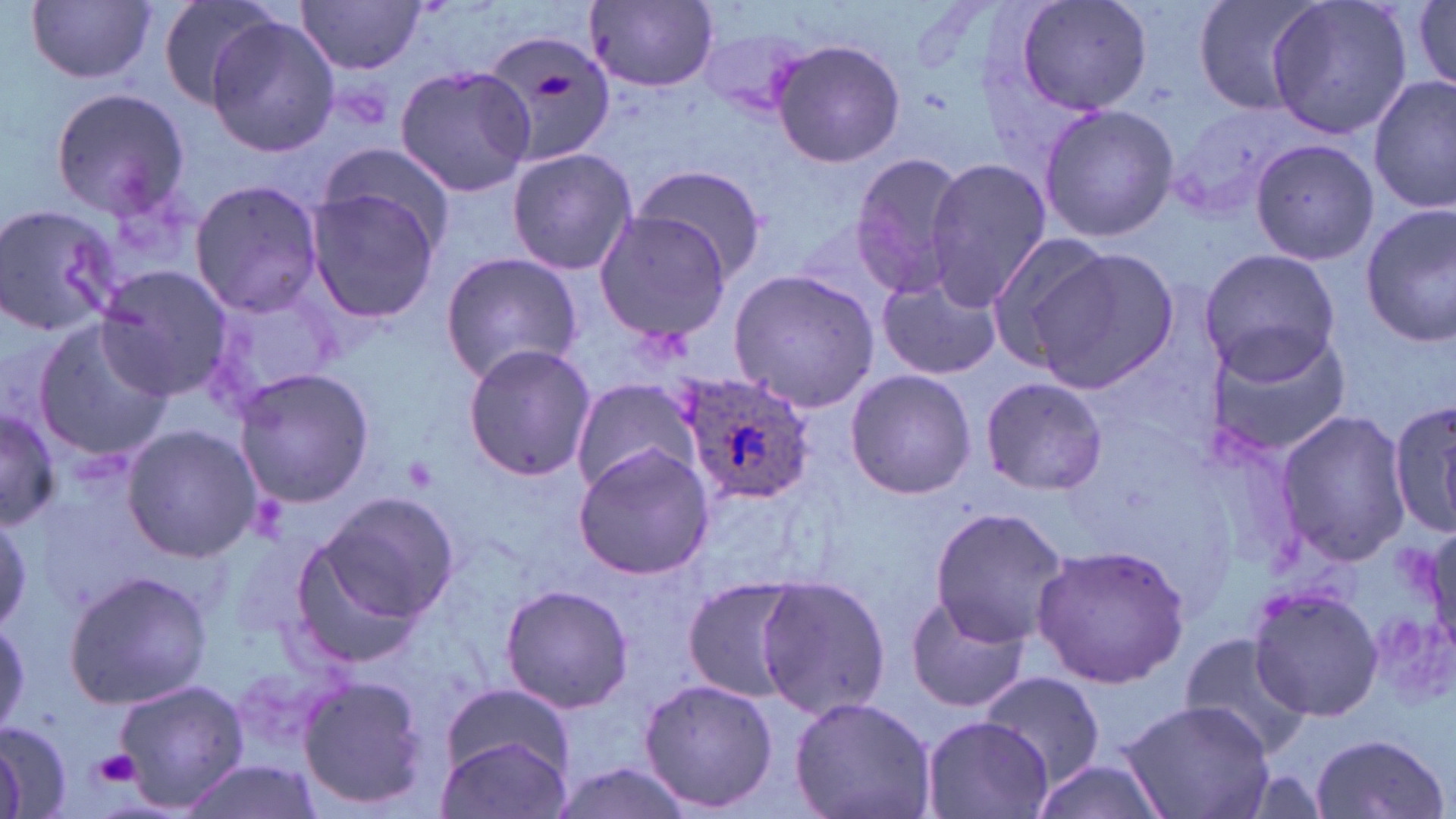

slide-level diagnosis = Plasmodium ovale
uninfected red blood cell locations = approximate bounding boxes as named x1/y1/x2/y2 corners in pixels: (x1=26, y1=0, x2=156, y2=84), (x1=154, y1=0, x2=283, y2=111), (x1=1014, y1=0, x2=1153, y2=119), (x1=1190, y1=0, x2=1326, y2=118), (x1=1263, y1=0, x2=1414, y2=140), (x1=297, y1=1, x2=428, y2=73), (x1=585, y1=1, x2=720, y2=90), (x1=1411, y1=1, x2=1456, y2=91), (x1=204, y1=16, x2=337, y2=159), (x1=482, y1=28, x2=621, y2=171), (x1=771, y1=38, x2=906, y2=168), (x1=394, y1=63, x2=536, y2=199), (x1=1370, y1=74, x2=1455, y2=214), (x1=47, y1=87, x2=191, y2=219), (x1=1037, y1=102, x2=1178, y2=243), (x1=1249, y1=138, x2=1379, y2=266), (x1=315, y1=146, x2=455, y2=260), (x1=506, y1=146, x2=637, y2=277), (x1=849, y1=151, x2=973, y2=297), (x1=924, y1=159, x2=1052, y2=308), (x1=628, y1=162, x2=769, y2=281), (x1=189, y1=178, x2=326, y2=318), (x1=305, y1=184, x2=443, y2=322), (x1=0, y1=201, x2=124, y2=337), (x1=1360, y1=206, x2=1456, y2=346), (x1=595, y1=211, x2=734, y2=342), (x1=981, y1=230, x2=1118, y2=367), (x1=1197, y1=247, x2=1343, y2=382), (x1=1027, y1=248, x2=1177, y2=393), (x1=439, y1=249, x2=585, y2=385), (x1=95, y1=266, x2=234, y2=401), (x1=726, y1=267, x2=881, y2=412), (x1=877, y1=277, x2=1001, y2=381), (x1=202, y1=282, x2=345, y2=411), (x1=31, y1=312, x2=175, y2=462), (x1=1203, y1=325, x2=1353, y2=460), (x1=462, y1=343, x2=595, y2=482), (x1=231, y1=368, x2=376, y2=508), (x1=845, y1=369, x2=977, y2=500), (x1=571, y1=376, x2=699, y2=495), (x1=979, y1=376, x2=1106, y2=495), (x1=1386, y1=399, x2=1456, y2=540), (x1=1, y1=404, x2=60, y2=531), (x1=1275, y1=408, x2=1412, y2=568), (x1=122, y1=424, x2=263, y2=561), (x1=572, y1=444, x2=715, y2=580), (x1=300, y1=489, x2=458, y2=648), (x1=927, y1=507, x2=1068, y2=649), (x1=0, y1=508, x2=31, y2=636), (x1=1031, y1=544, x2=1191, y2=688), (x1=64, y1=568, x2=211, y2=709), (x1=755, y1=573, x2=889, y2=722), (x1=682, y1=577, x2=803, y2=702), (x1=498, y1=583, x2=633, y2=714), (x1=1248, y1=585, x2=1384, y2=721), (x1=904, y1=593, x2=1028, y2=714), (x1=1179, y1=633, x2=1313, y2=760), (x1=980, y1=670, x2=1105, y2=787), (x1=297, y1=674, x2=433, y2=810), (x1=113, y1=677, x2=249, y2=813), (x1=637, y1=677, x2=777, y2=815), (x1=441, y1=682, x2=577, y2=784), (x1=790, y1=695, x2=937, y2=819), (x1=1118, y1=699, x2=1275, y2=819), (x1=921, y1=715, x2=1055, y2=819), (x1=0, y1=719, x2=71, y2=818), (x1=1309, y1=732, x2=1450, y2=819), (x1=436, y1=734, x2=571, y2=819), (x1=548, y1=759, x2=702, y2=819), (x1=178, y1=760, x2=321, y2=819), (x1=1029, y1=760, x2=1171, y2=819)
platelet locations = approximate bounding boxes as named x1/y1/x2/y2 corners in pixels: (x1=531, y1=72, x2=575, y2=98), (x1=93, y1=749, x2=140, y2=787)
Plasmodium ovale-infected red blood cell locations = approximate bounding boxes as named x1/y1/x2/y2 corners in pixels: (x1=678, y1=369, x2=815, y2=506)
modality = light microscopy
preparation = thin blood film
stain = May-Grünwald-Giemsa
magnification = 1000x
image size = 1456×819 pixels
field of view = one of a larger specimen